Assess this cell for malaria.
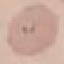

Uninfected.

preparation = thin smear
capture = smartphone through the microscope eyepiece
stain = Giemsa
image type = cell patch, automatically extracted from a larger field of view and resized to 64 × 64 pixels